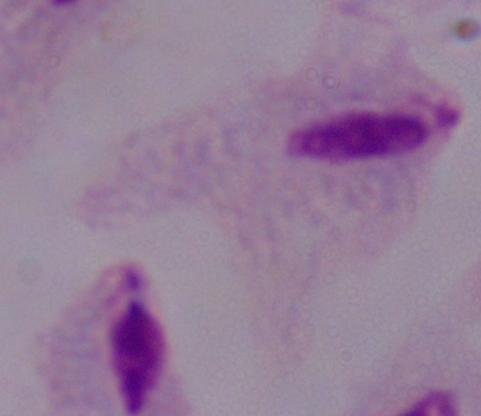

Summary:
  - Modality: photomicrograph
  - Identification: trichomonad
  - Magnification: 1000x